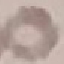

Result: no malaria parasites detected. Automatically extracted cell patch, resized to 64 × 64 pixels. Thin blood smear. Giemsa stain. Photographed with a smartphone camera at the microscope eyepiece.